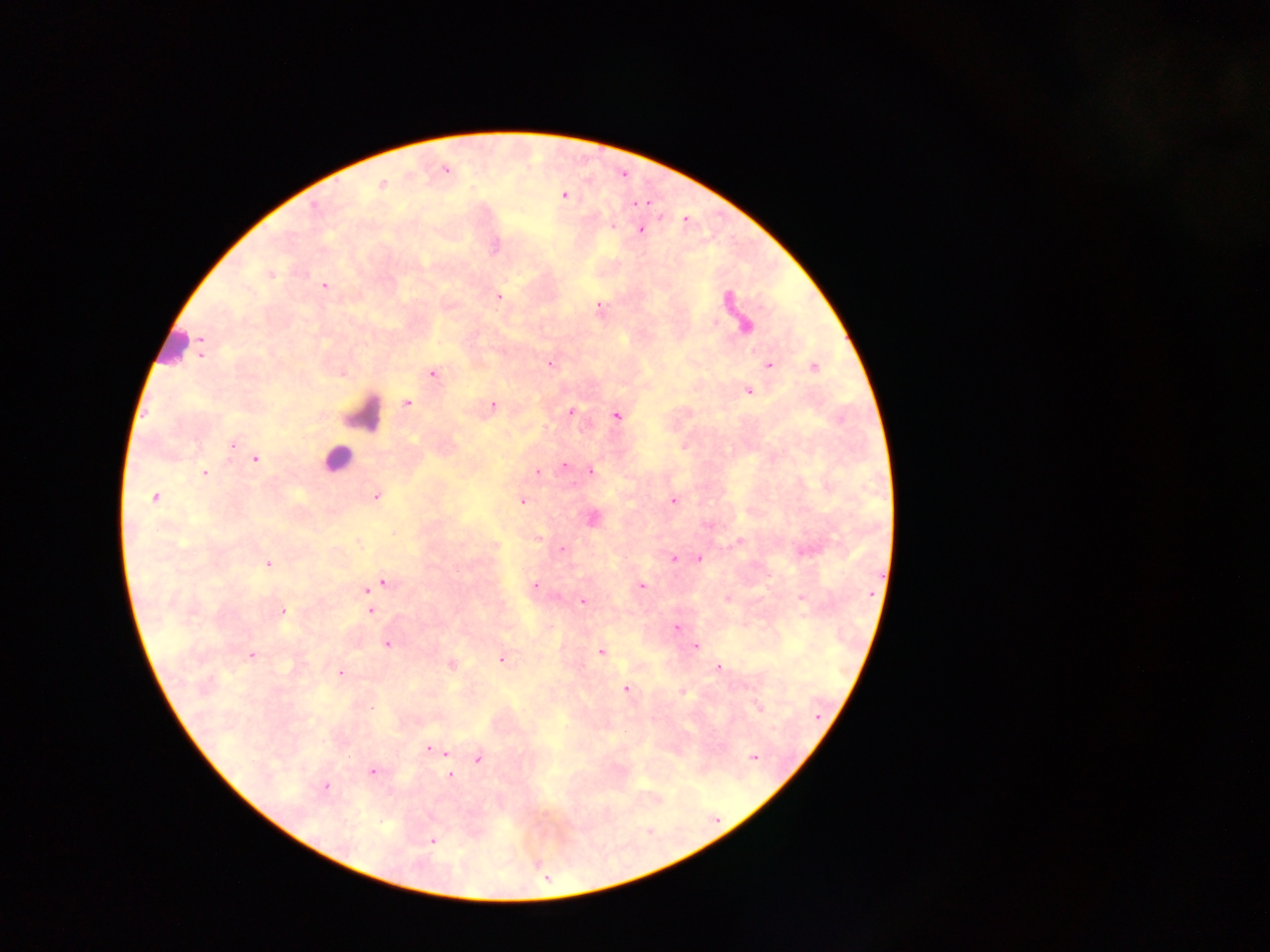

Approximate centers as {x, y} in pixels. Leukocyte locations: {171, 344}, {361, 414}, {337, 458}. Malaria parasite locations: {444, 169}, {382, 184}, {565, 195}, {613, 226}, {640, 229}, {270, 274}, {324, 285}, {497, 296}, {598, 307}, {746, 326}, {201, 349}, {550, 364}, {768, 365}, {814, 367}, {432, 373}, {748, 391}, {407, 402}, {493, 405}, {570, 412}, {615, 415}, {233, 445}, {684, 446}, {255, 458}, {566, 465}, {589, 471}, {536, 472}, {203, 473}, {376, 496}, {155, 497}, {672, 500}, {522, 501}, {591, 518}, {708, 525}, {393, 533}, {537, 538}, {739, 542}, {495, 546}, {561, 549}, {673, 558}, {698, 558}, {268, 564}, {382, 582}, {534, 584}, {641, 586}, {367, 588}, {726, 597}, {800, 597}, {582, 601}, {370, 609}, {281, 611}, {677, 628}, {387, 644}, {694, 645}, {601, 651}, {251, 654}, {501, 659}, {450, 664}, {718, 667}, {339, 673}, {625, 688}, {682, 691}, {757, 707}, {429, 749}, {446, 752}, {753, 757}, {477, 758}, {371, 771}, {448, 775}, {324, 787}, {432, 840}. Thick blood smear. Image is 1270×952 pixels. Single field of view. Collected in Ghana. Photographed through a microscope with a mobile-phone camera.